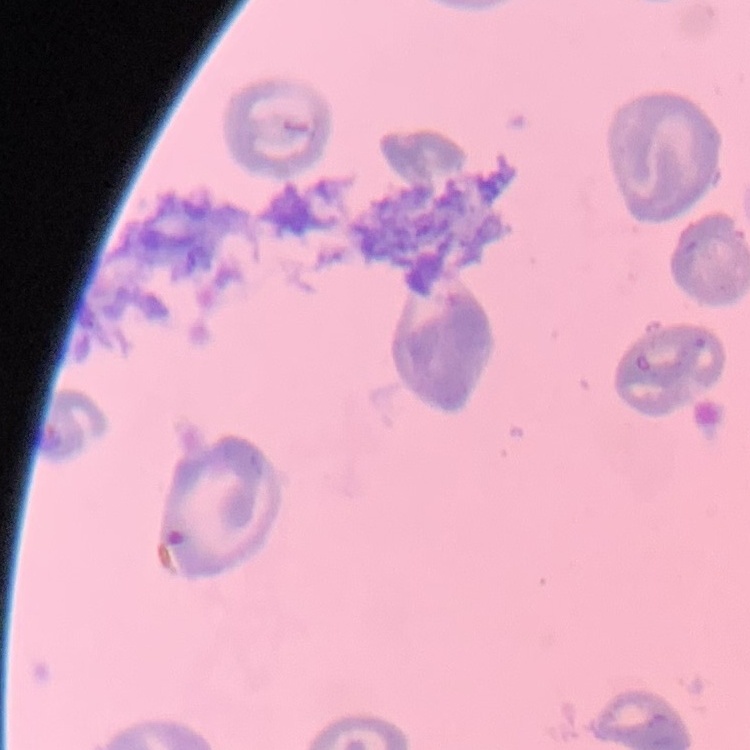
erythrocyte_morphology: no rouleaux formation
preparation: thin peripheral smear
image_type: square crop of a larger photomicrograph
stain: Field's or Giemsa